Point out each Plasmodium parasite and each leukocyte.
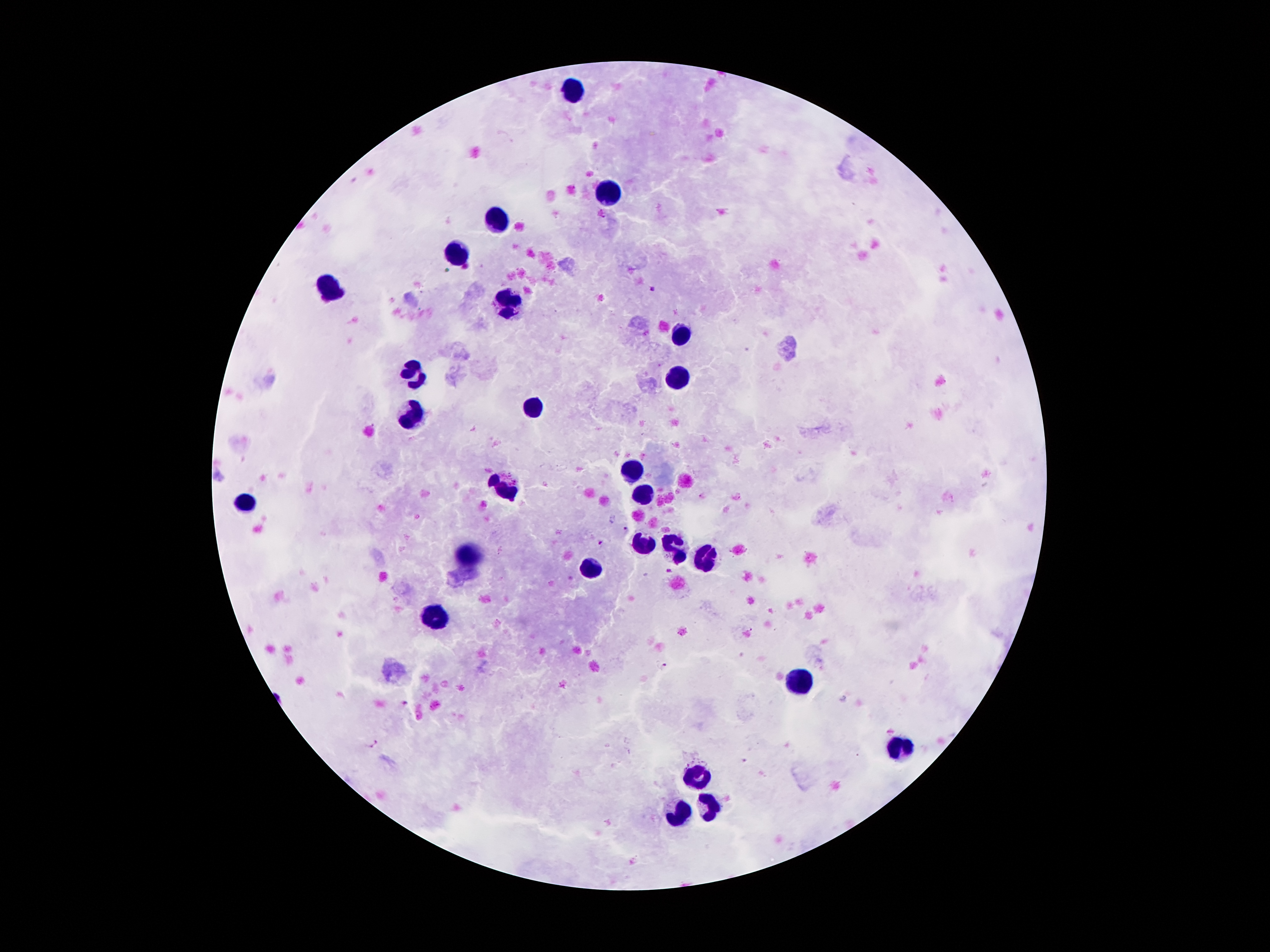

Approximate object centers, in pixels from the top-left corner.
Plasmodium parasites: (x=651, y=289), (x=626, y=528), (x=600, y=544), (x=669, y=571), (x=664, y=664), (x=404, y=703), (x=374, y=743), (x=744, y=760).
Leukocytes: (x=576, y=91), (x=606, y=196), (x=499, y=221), (x=458, y=253), (x=333, y=292), (x=508, y=306), (x=683, y=337), (x=678, y=372), (x=415, y=375), (x=535, y=409), (x=409, y=418), (x=633, y=468), (x=504, y=485), (x=644, y=493), (x=245, y=502), (x=640, y=543), (x=677, y=548), (x=468, y=555), (x=704, y=558), (x=588, y=568), (x=432, y=617), (x=800, y=679), (x=899, y=748), (x=696, y=775), (x=706, y=808), (x=680, y=815).

100x magnification. Single field of view. Image is 1270×952 pixels. Photographed through the microscope eyepiece with a smartphone camera. Patient malaria status: infected with Plasmodium falciparum. Giemsa-stained preparation. Thick peripheral-blood smear.